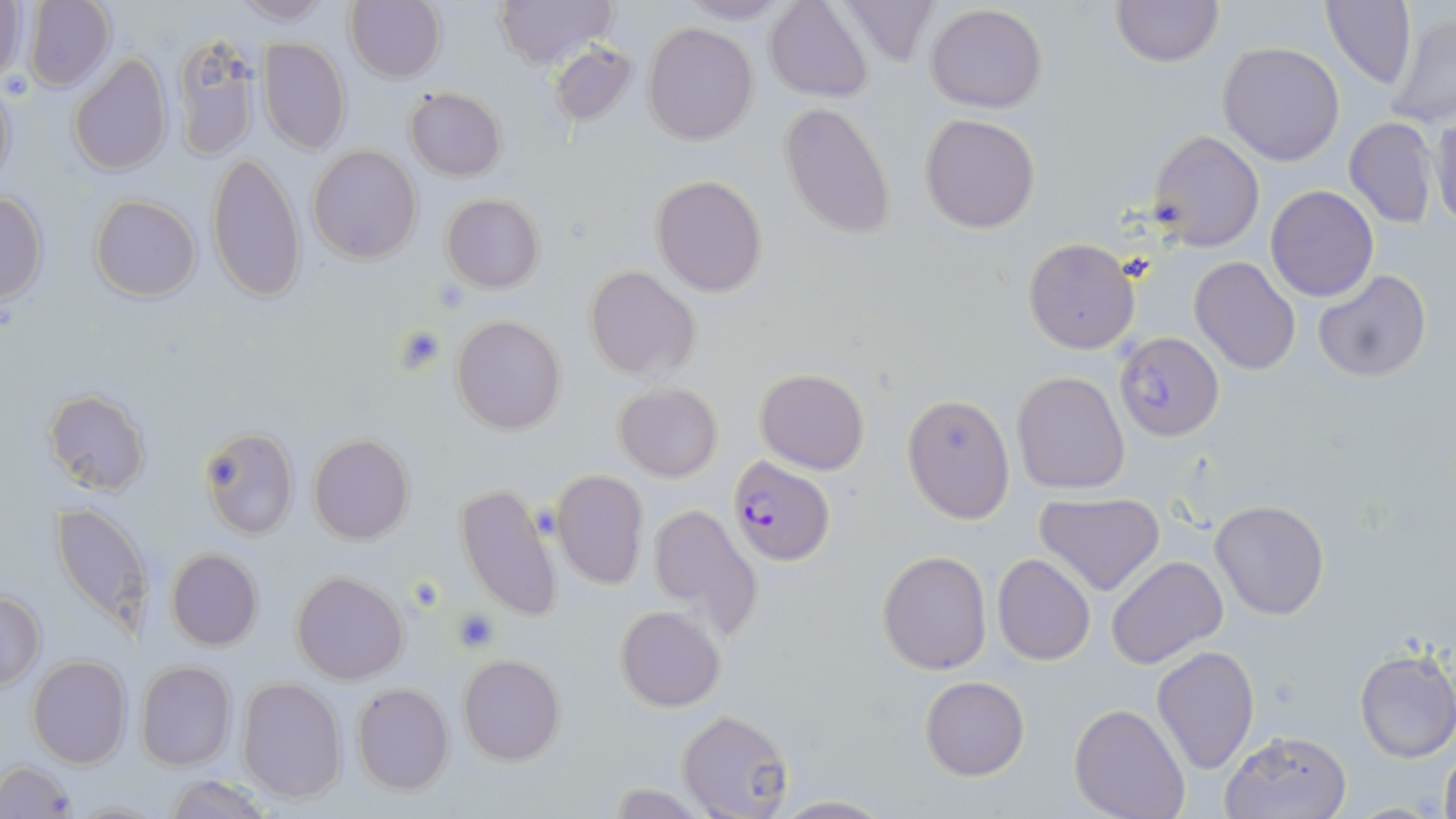
Summary:
  - Coordinate format: approximate bounding boxes as (x1,y1)-(x2,y2) corner pairs in pixels
  - Uninfected red blood cell locations: (227,0)-(338,26), (492,0)-(618,69), (676,0)-(798,23), (840,0)-(944,67), (1111,0)-(1223,67), (22,1)-(114,93), (345,1)-(444,83), (764,1)-(875,102), (0,2)-(27,82), (1321,2)-(1418,89), (926,4)-(1048,114), (1384,11)-(1456,130), (642,22)-(759,146), (170,35)-(261,162), (259,38)-(351,155), (549,41)-(638,128), (1218,42)-(1345,166), (69,54)-(171,175), (1,77)-(17,196), (404,86)-(507,182), (778,102)-(897,240), (1427,110)-(1456,231), (919,113)-(1040,234), (1342,117)-(1438,229), (1148,129)-(1265,252), (308,145)-(421,265), (206,152)-(306,305), (650,174)-(769,297), (1265,185)-(1378,301), (0,192)-(48,303), (441,194)-(544,293), (90,195)-(201,302), (1024,238)-(1140,355), (1190,257)-(1300,374), (583,266)-(701,382), (1313,269)-(1431,383), (451,314)-(569,434), (754,368)-(870,476), (1010,370)-(1130,495), (613,382)-(723,482), (44,390)-(150,495), (901,393)-(1015,523), (197,425)-(299,541), (308,434)-(414,544), (551,469)-(650,590), (454,483)-(564,623), (1037,492)-(1165,595), (1209,498)-(1330,620), (50,499)-(151,637), (646,502)-(764,640), (165,548)-(264,651), (877,550)-(993,675), (991,553)-(1095,666), (1106,555)-(1227,668), (291,570)-(409,684), (1,590)-(45,690), (615,606)-(725,712), (1152,644)-(1259,775), (1354,647)-(1456,762), (458,653)-(566,766), (27,655)-(131,769), (137,661)-(236,770), (919,675)-(1029,781), (237,677)-(348,803), (351,682)-(455,795), (1071,702)-(1190,819), (676,708)-(794,819), (1219,729)-(1351,818), (1439,744)-(1456,819), (1,760)-(76,817), (163,774)-(272,819), (766,794)-(896,818)
  - Platelet locations: (394,327)-(449,375), (452,607)-(502,652)
  - Plasmodium falciparum-infected red blood cell locations: (1113,331)-(1225,440), (727,455)-(836,566)
  - Slide-level diagnosis: Plasmodium falciparum
  - Preparation: thin blood smear
  - Stain: May-Grünwald-Giemsa
  - Magnification: 1000x
  - Field of view: single
  - Image size: 1456×819 pixels
  - Modality: optical microscopy